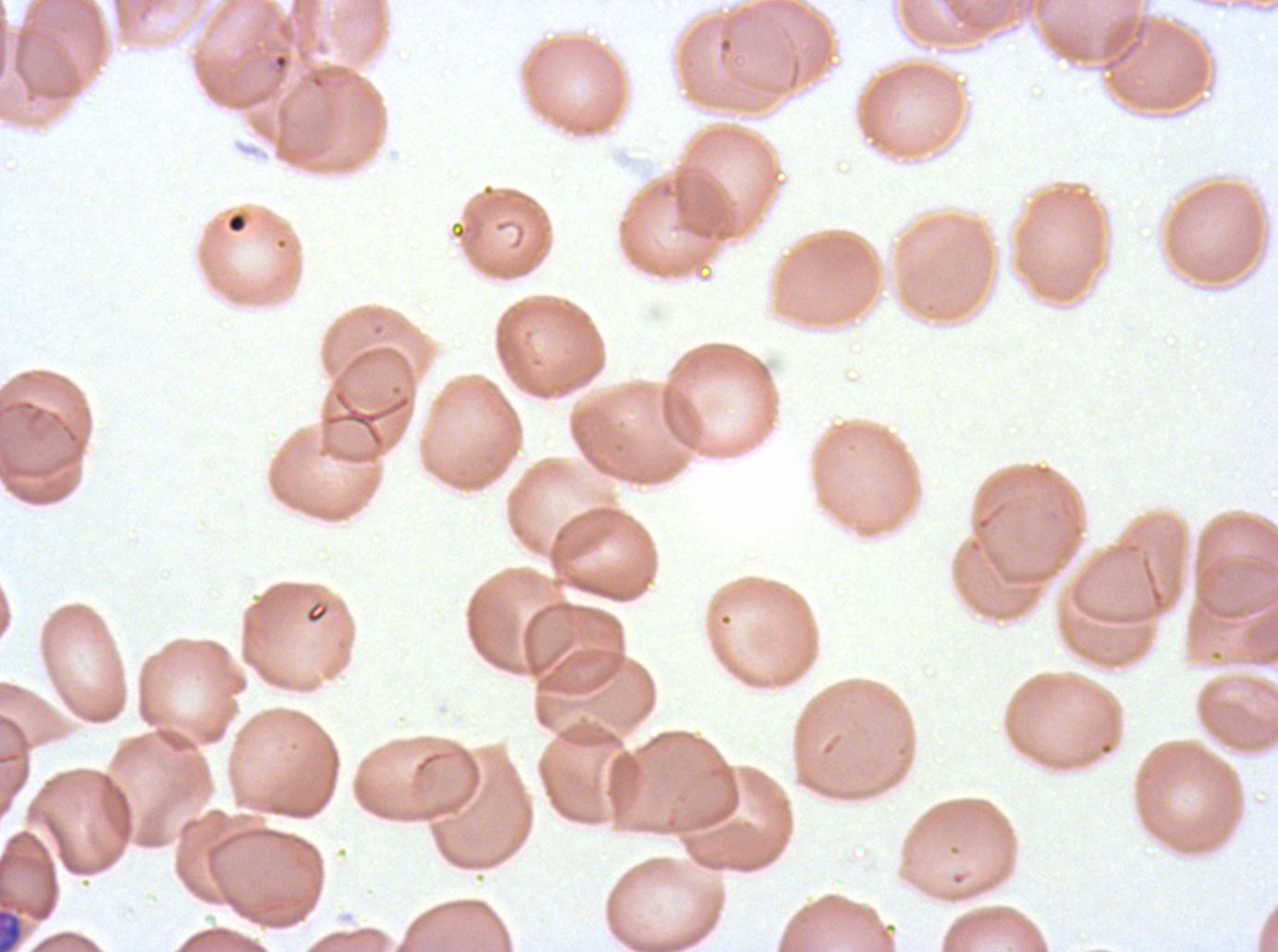

Approximate bounding boxes as (x1, y1, x2, y2) in pixels.
Summary:
  - Late schizont locations: (0, 909, 22, 951)
  - Stain: Giemsa
  - Field of view: one sub-image of a larger composite
  - Image size: 1278×952 pixels
  - Preparation: thin blood smear
  - Specimen: P. falciparum from a patient in The Gambia, cultured ex vivo for 24 to 48 hours